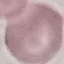
Summary:
  - Malaria status: uninfected
  - Image type: cell patch, automatically extracted from a larger field of view and resized to 64 × 64 pixels
  - Preparation: thin blood smear
  - Capture: smartphone camera at the microscope eyepiece
  - Stain: Giemsa